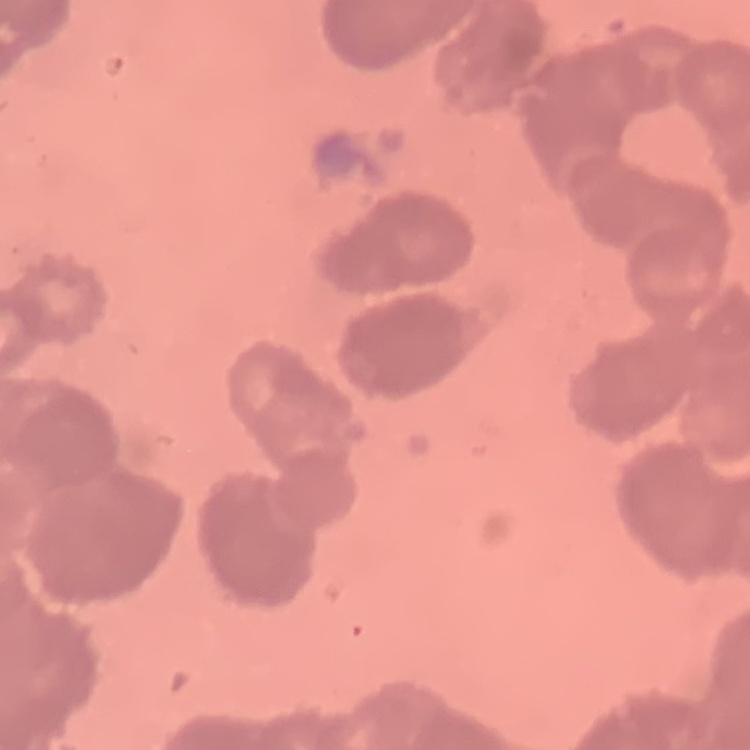

Summary:
  - Red blood cell morphology: rouleaux formation
  - Image type: square crop of a larger photomicrograph
  - Preparation: thin blood film
  - Stain: Field's or Giemsa